Name the cell type shown.
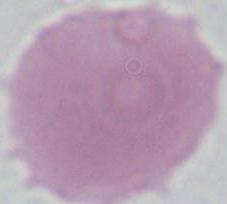
An erythrocyte.

Summary:
  - Modality: photomicrograph
  - Magnification: 1000x